Classify this cell by malaria status.
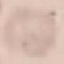

It is uninfected.

Summary:
  - Preparation: thin blood film
  - Image type: cell patch, automatically extracted from a larger field of view and resized to 64 × 64 pixels
  - Capture: smartphone through the microscope eyepiece
  - Stain: Giemsa